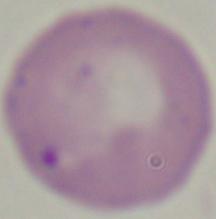

Summary:
  - Magnification: 1000x
  - Identification: Babesia
  - Modality: photomicrograph